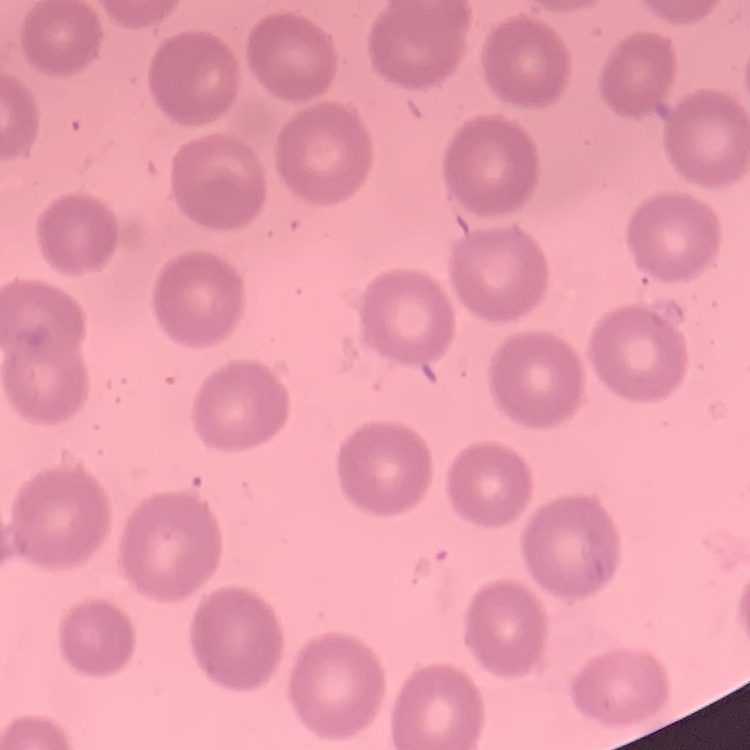
erythrocyte_morphology: no rouleaux formation
image_type: square crop of a larger photomicrograph
preparation: thin peripheral smear
stain: Field's or Giemsa